Give the position of every leukocyte visible.
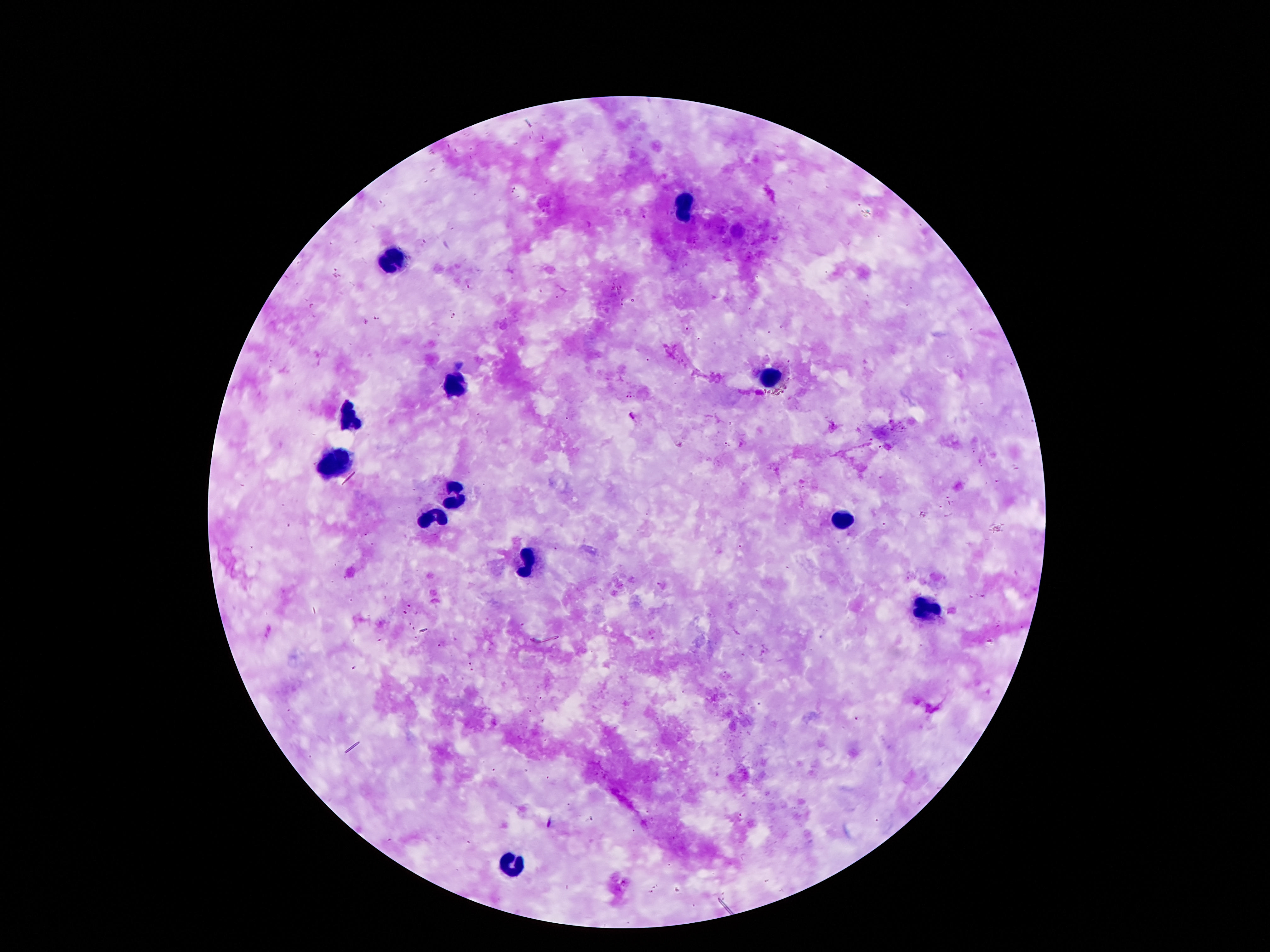

Approximate centers as {x, y} in pixels.
Leukocytes: {684, 205}, {391, 259}, {770, 379}, {458, 388}, {350, 419}, {328, 464}, {455, 496}, {427, 520}, {841, 520}, {527, 565}, {927, 607}, {511, 866}.

Summary:
  - Image size: 1270×952 pixels
  - Patient malaria status: uninfected
  - Capture: smartphone camera through the microscope eyepiece
  - Field of view: single
  - Magnification: 100x
  - Preparation: thick blood film
  - Stain: Giemsa